Assess this cell for malaria.
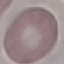

Uninfected.

{
  "image_type": "cell patch, automatically extracted from a larger field of view and resized to 64 × 64 pixels",
  "preparation": "thin blood smear",
  "stain": "Giemsa",
  "capture": "smartphone camera at the microscope eyepiece"
}